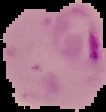

Summary:
  - Image type: segmented cell region on a black background
  - Preparation: thin blood film
  - Result: Plasmodium parasites detected
  - Image size: 106×112 pixels